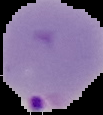

image size = 103×115 pixels
image type = segmented cell region with the area outside set to black
preparation = thin blood film
result = malaria parasites detected